Classify this cell by malaria status.
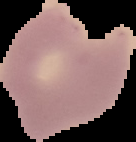

Parasitized.

Image is 136×142 pixels. From a thin blood film. The area outside the segmented cell region is set to black.